Identify the preparation type.
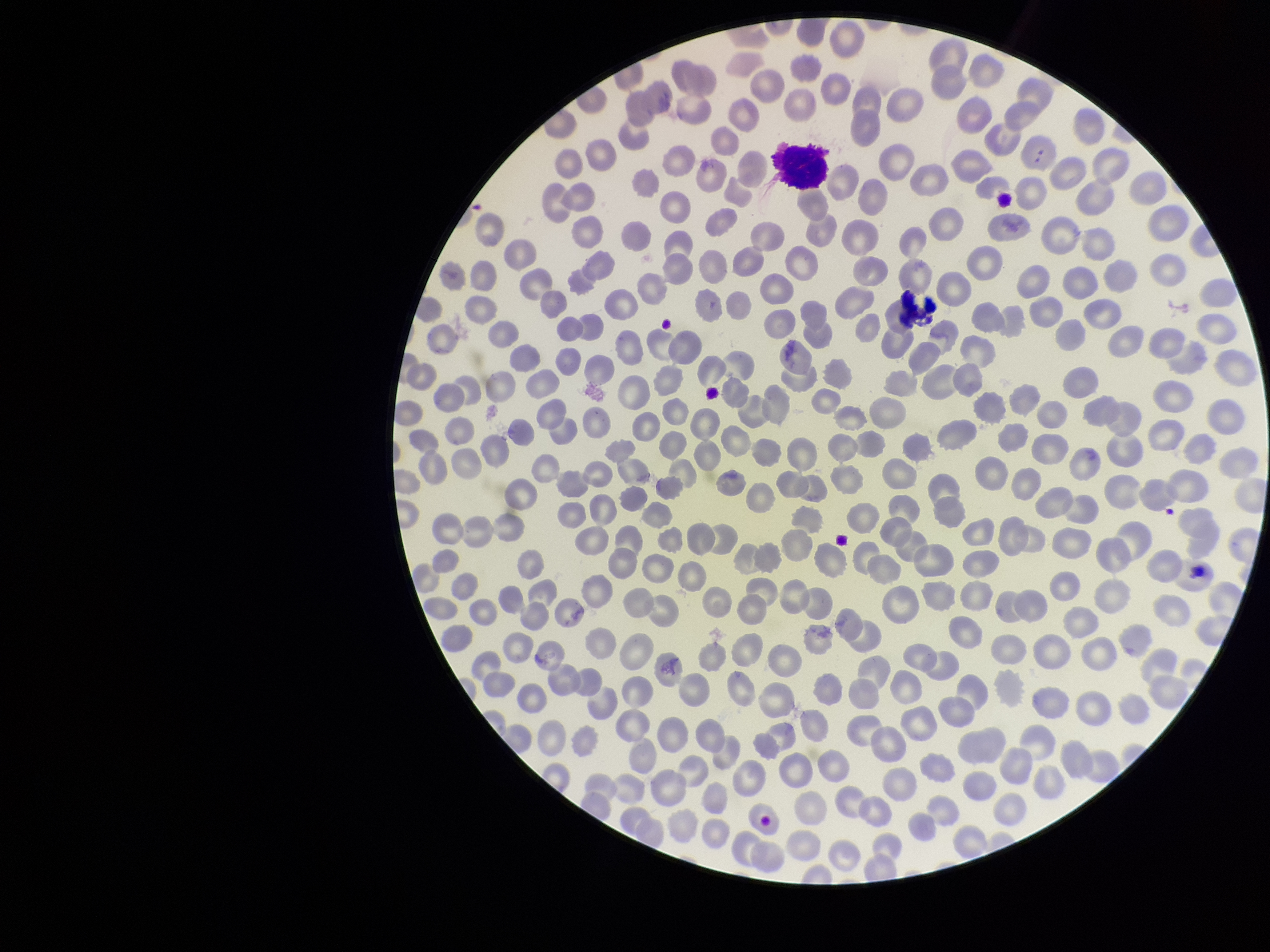

A thin smear.

Smartphone photograph taken through the eyepiece of a microscope. Parasitized red blood cells: none identified. Red blood cell count: 317. Image is 1270×952 pixels. Species reported for this patient: Plasmodium vivax. Patient malaria status: positive. Parasitized red blood cell count: 0. Stained with Giemsa. Single field of view.